Outline each Plasmodium malariae-infected red blood cell.
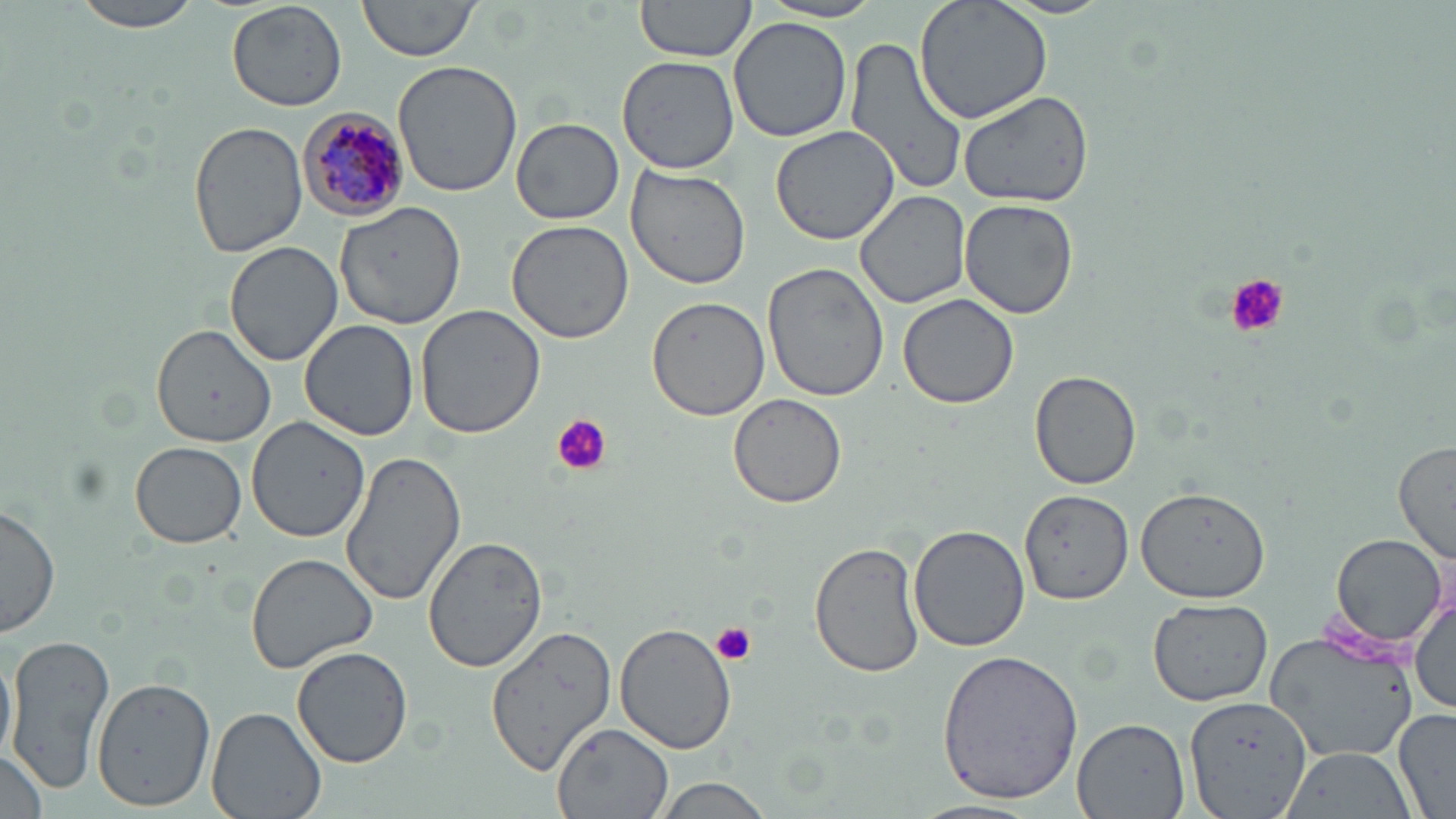
Approximate bounding boxes as (x1,y1)-(x2,y2) corner pairs in pixels.
Plasmodium malariae-infected red blood cells: (298,106)-(415,222).

slide_level_diagnosis: Plasmodium malariae
magnification: 1000x
field_of_view: one of a larger specimen
uninfected_red_blood_cell_locations: 'approximate bounding boxes as (x1,y1)-(x2,y2) corner pairs in pixels: (70,0)-(201,33), (227,0)-(347,113), (358,0)-(482,62), (634,0)-(759,63), (762,0)-(887,23), (915,0)-(1052,124), (728,17)-(852,143), (844,36)-(968,199), (615,55)-(739,173), (394,58)-(524,198), (956,88)-(1096,210), (513,118)-(623,225), (188,122)-(307,257), (769,126)-(901,246), (625,164)-(752,292), (855,191)-(971,309), (959,199)-(1078,319), (334,202)-(469,330), (505,219)-(634,344), (225,242)-(342,367), (762,261)-(892,401), (898,292)-(1021,409), (646,297)-(769,422), (414,304)-(549,437), (147,318)-(270,467), (300,319)-(418,441), (1029,370)-(1140,490), (729,393)-(848,508), (248,416)-(371,541), (130,442)-(248,549), (1392,442)-(1455,562), (338,451)-(465,607), (1136,481)-(1269,628), (1021,489)-(1132,603), (0,503)-(60,637), (909,522)-(1031,651), (422,534)-(549,674), (1329,534)-(1447,650), (811,539)-(924,679), (246,553)-(378,673), (1410,586)-(1455,717), (1147,598)-(1273,707), (616,622)-(739,755), (484,623)-(621,773), (1264,629)-(1417,764), (5,632)-(115,795), (0,640)-(16,772), (293,647)-(413,768), (935,648)-(1086,805), (91,677)-(215,811), (1186,695)-(1314,819), (206,706)-(328,819), (1393,709)-(1455,819), (1072,719)-(1188,819), (551,722)-(674,819), (1,745)-(49,819), (1277,748)-(1417,819), (648,777)-(774,818), (910,800)-(1043,819)'
image_size: 1456×819 pixels
platelet_locations: 'approximate bounding boxes as (x1,y1)-(x2,y2) corner pairs in pixels: (1223,274)-(1289,337), (551,414)-(611,475), (712,622)-(757,665)'
modality: optical microscopy
stain: May-Grünwald-Giemsa
preparation: thin blood film